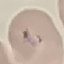

malaria status = uninfected
capture = smartphone through the microscope eyepiece
preparation = thin smear
stain = Giemsa
image type = automatically extracted cell patch, resized to 64 × 64 pixels